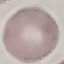
Summary:
  - Malaria status: uninfected
  - Image type: cell patch, automatically extracted from a larger field of view and resized to 64 × 64 pixels
  - Preparation: thin smear
  - Stain: Giemsa
  - Capture: smartphone through the microscope eyepiece